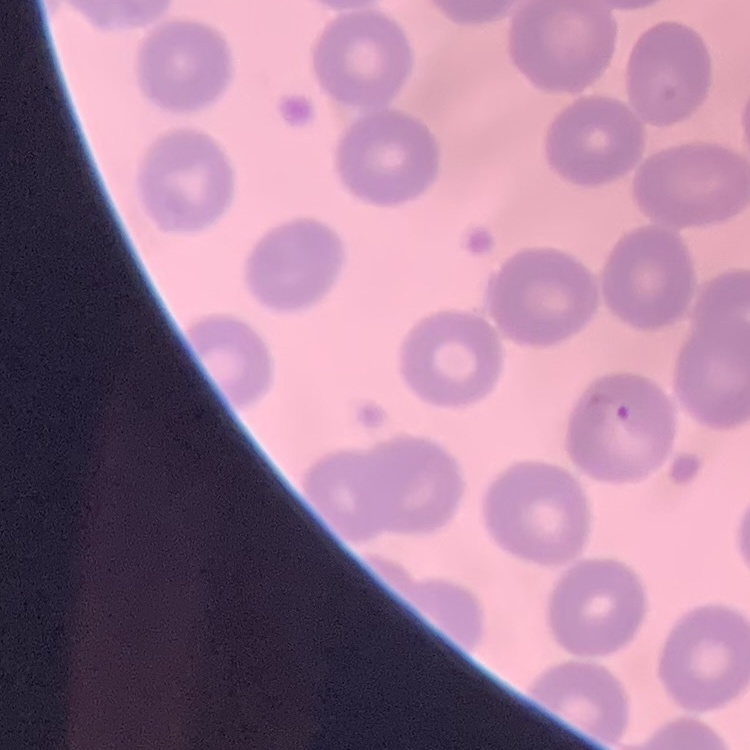
The erythrocytes show no rouleaux formation. One tile cut from a larger photomicrograph. Thin blood smear. Stained with either Field's or Giemsa.